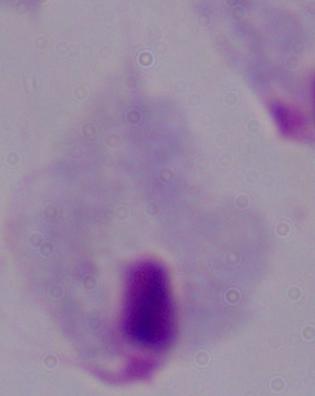
Summary:
  - Modality: photomicrograph
  - Identification: trichomonad
  - Magnification: 1000x